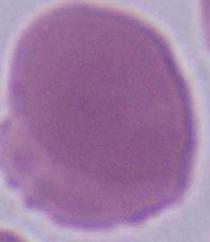

Summary:
  - Identification: red blood cell
  - Magnification: 1000x
  - Modality: photomicrograph